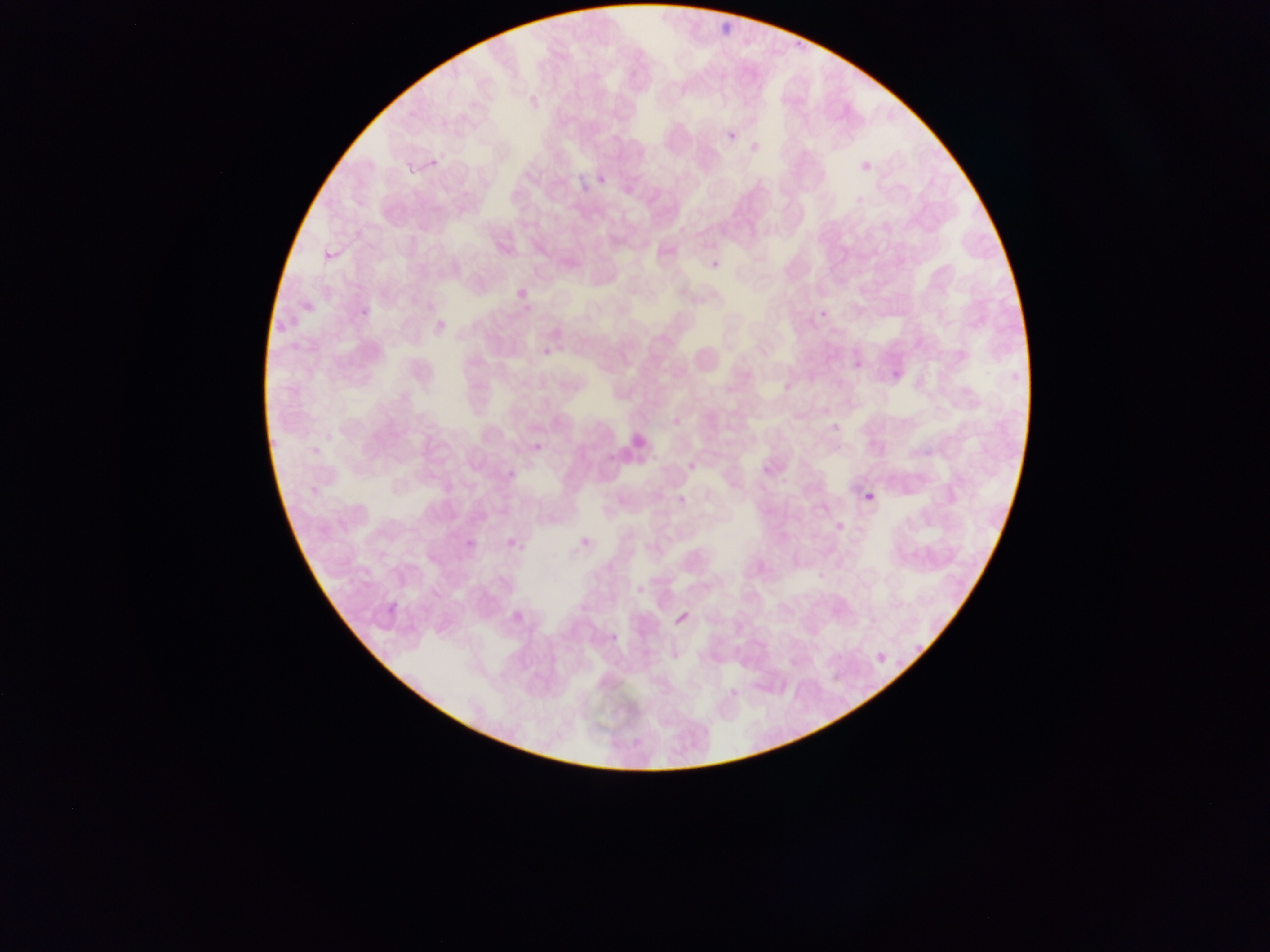 Approximate bounding boxes as [left, top, right, bottom] in pixels. Malaria parasite locations: [718, 7, 743, 40], [724, 107, 755, 143], [594, 160, 612, 183], [582, 163, 600, 189], [321, 229, 341, 258], [703, 249, 730, 267], [506, 282, 530, 299], [291, 298, 309, 312], [813, 298, 836, 320], [287, 311, 310, 332], [264, 316, 284, 342], [850, 338, 872, 370], [535, 343, 555, 360], [884, 367, 909, 386], [771, 376, 793, 395], [825, 411, 850, 431], [526, 438, 547, 464], [500, 462, 518, 481], [863, 489, 879, 509], [827, 499, 856, 534], [456, 523, 478, 551], [577, 528, 584, 548], [502, 529, 520, 554], [505, 598, 525, 625], [666, 606, 698, 633], [603, 624, 628, 646], [910, 634, 928, 657], [871, 643, 893, 663]. Leukocyte locations: [685, 337, 733, 413], [606, 428, 655, 476]. Collected in Ghana. One field of view. Mobile-phone photograph taken through the microscope. Image is 1270×952 pixels. Thin blood film.